Identify the parasite.
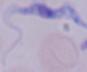
This is a trypanosome.

{
  "magnification": "1000x",
  "modality": "photomicrograph"
}